State which parasite is depicted.
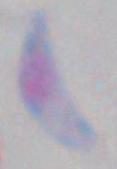
This is Toxoplasma gondii.

magnification = 1000x
modality = photomicrograph